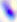
Summary:
  - Modality: photomicrograph
  - Magnification: 400x
  - Identification: Toxoplasma gondii